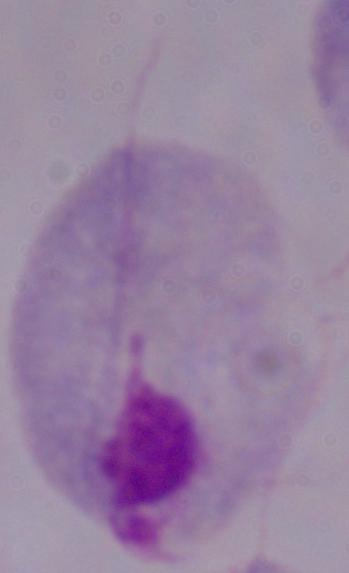
1000x magnification. A trichomonad is shown. Micrograph.